Locate every uninfected red blood cell.
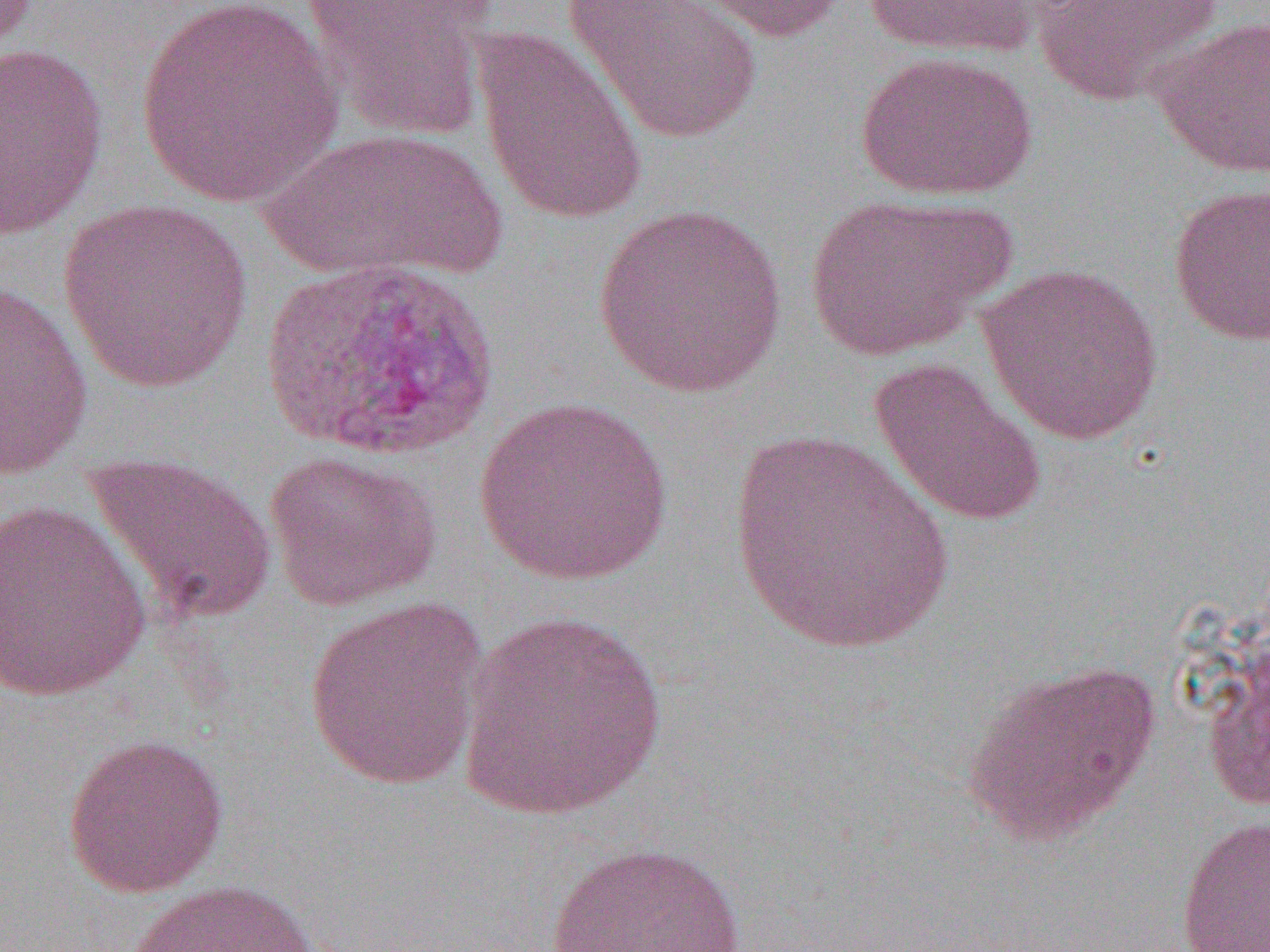
Approximate bounding boxes as (x1,y1)-(x2,y2) corner pairs in pixels.
Uninfected red blood cells: (562,0)-(763,145), (664,0)-(851,42), (856,0)-(1064,60), (1033,0)-(1225,106), (298,1)-(497,141), (131,2)-(345,208), (1149,14)-(1270,179), (472,27)-(649,226), (0,41)-(110,241), (856,52)-(1037,201), (254,126)-(510,285), (1167,182)-(1270,346), (801,192)-(1015,361), (57,198)-(254,393), (591,202)-(789,397), (976,262)-(1164,446), (0,278)-(94,481), (868,355)-(1047,529), (474,395)-(676,584), (727,428)-(956,658), (265,449)-(441,611), (82,451)-(276,627), (1,499)-(153,702), (302,594)-(492,791), (455,611)-(670,819), (961,658)-(1161,846), (62,731)-(229,898), (1174,815)-(1270,952), (539,841)-(752,952), (125,879)-(320,952).

Slide-level diagnosis: Plasmodium vivax. One field of a larger specimen. Thin blood film. Light microscopy. Captured at 1000x magnification. Image is 1270×952 pixels.